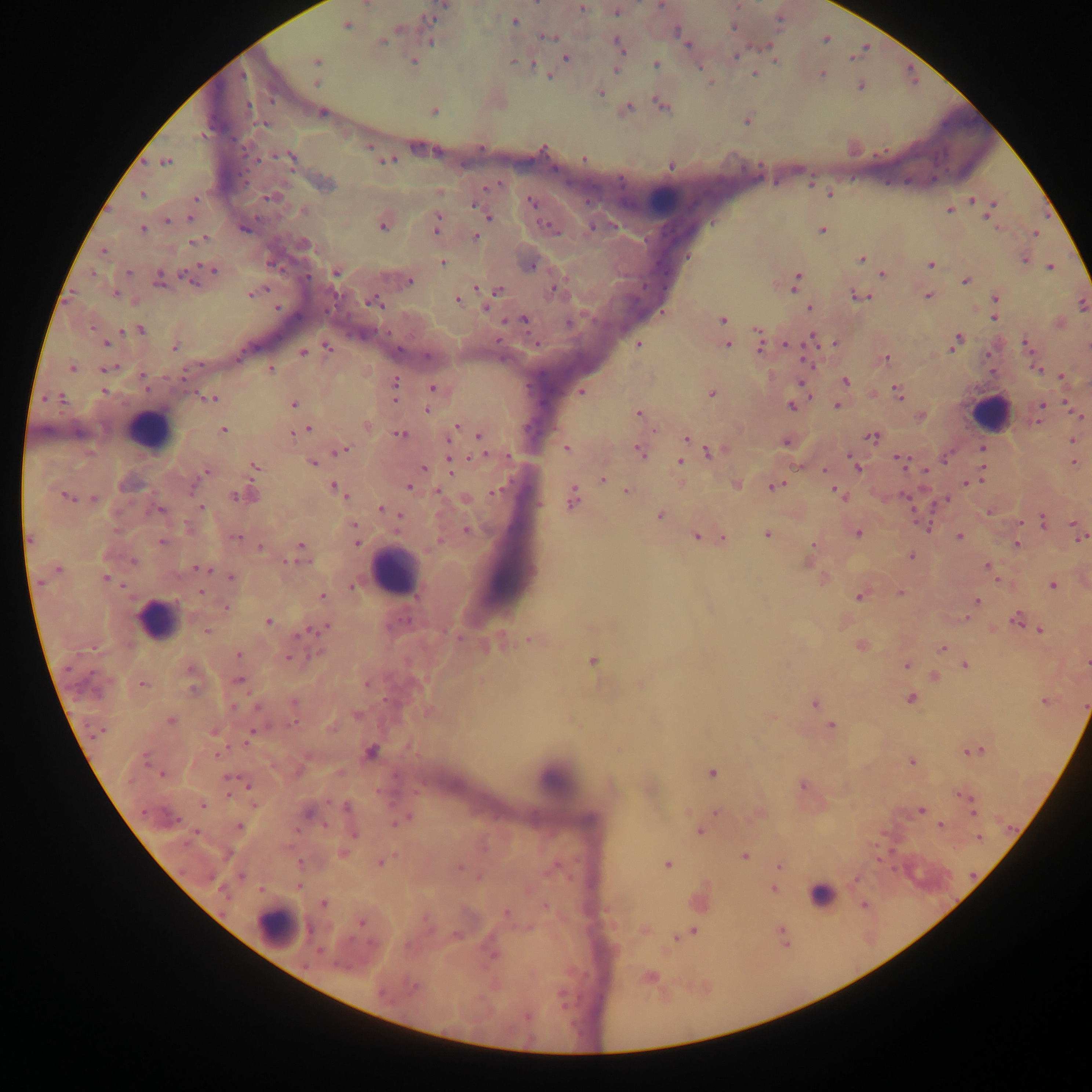 Approximate centers as [x, y] in pixels. Leukocyte locations: [663, 200], [989, 413], [149, 430], [393, 571], [158, 619], [822, 894], [277, 928]. Plasmodium parasite locations: [366, 4], [660, 5], [442, 6], [581, 8], [617, 11], [432, 19], [515, 21], [346, 26], [733, 27], [678, 33], [548, 37], [825, 39], [382, 42], [431, 42], [686, 43], [619, 44], [735, 55], [566, 59], [776, 60], [316, 61], [413, 62], [514, 62], [655, 65], [617, 69], [754, 74], [822, 75], [549, 78], [317, 83], [861, 86], [601, 92], [662, 105], [628, 109], [434, 111], [322, 112], [747, 121], [264, 124], [370, 146], [290, 158], [583, 159], [387, 160], [166, 162], [671, 166], [491, 187], [142, 194], [829, 194], [272, 197], [195, 198], [973, 200], [531, 201], [475, 205], [992, 205], [303, 211], [949, 211], [488, 215], [989, 216], [190, 219], [167, 221], [383, 226], [436, 226], [594, 226], [244, 228], [550, 228], [142, 229], [822, 230], [1035, 234], [476, 237], [198, 240], [103, 251], [861, 258], [1025, 260], [443, 263], [931, 265], [531, 266], [1050, 267], [214, 270], [128, 273], [336, 273], [882, 273], [93, 274], [184, 276], [158, 280], [966, 280], [409, 281], [796, 282], [554, 289], [498, 290], [116, 293], [253, 293], [859, 295], [928, 295], [996, 298], [458, 300], [374, 303], [1082, 305], [277, 308], [485, 308], [809, 309], [663, 312], [995, 317], [722, 320], [524, 321], [568, 323], [140, 330], [757, 330], [811, 339], [105, 343], [834, 343], [956, 343], [760, 344], [1026, 344], [638, 345], [728, 345], [786, 345], [175, 347], [327, 348], [304, 353], [426, 356], [238, 358], [887, 358], [71, 368], [106, 369], [1037, 369], [270, 370], [186, 373], [1061, 376], [144, 380], [846, 381], [395, 382], [146, 388], [433, 388], [395, 389], [103, 391], [581, 392], [899, 393], [712, 394], [53, 397], [46, 398], [61, 398], [211, 399], [395, 399], [294, 404], [837, 405], [1043, 405], [791, 406], [427, 410], [638, 414], [1078, 416], [920, 417], [367, 425], [456, 428], [309, 429], [223, 430], [295, 433], [401, 435], [479, 436], [686, 437], [872, 437], [1072, 440], [785, 443], [343, 449], [566, 449], [982, 449], [640, 451], [708, 452], [507, 456], [946, 458], [900, 460], [680, 462], [313, 463], [1074, 464], [451, 465], [255, 466], [855, 466], [424, 468], [824, 470], [206, 472], [926, 472], [980, 478], [602, 479], [967, 483], [736, 485], [775, 486], [409, 487], [334, 488], [497, 491], [627, 491], [439, 492], [253, 495], [841, 495], [65, 496], [239, 497], [573, 497], [93, 498], [945, 501], [201, 507], [382, 509], [160, 511], [989, 512], [398, 515], [660, 516], [1043, 521], [1073, 524], [354, 526], [925, 527], [467, 530], [857, 533], [768, 534], [697, 536], [236, 537], [960, 537], [1081, 538], [30, 539], [723, 539], [162, 541], [357, 543], [812, 545], [1016, 545], [302, 546], [261, 548], [911, 556], [133, 561], [987, 566], [200, 568], [58, 569], [231, 578], [105, 579], [1053, 586], [351, 587], [201, 593], [900, 593], [322, 596], [859, 597], [977, 601], [225, 608], [965, 619], [1016, 619], [268, 622], [317, 629], [1041, 630], [207, 632], [301, 633], [530, 639], [862, 646], [942, 649], [239, 655], [289, 657], [592, 661], [1087, 663], [906, 665], [965, 665], [191, 671], [934, 676], [238, 680], [143, 684], [367, 684], [193, 689], [911, 698], [1045, 701], [294, 703], [814, 703], [257, 707], [234, 708], [356, 715], [171, 721], [294, 722], [831, 725], [214, 731], [99, 732], [250, 735], [246, 741], [973, 750], [371, 752], [218, 754], [145, 760], [912, 762], [712, 772], [161, 774], [230, 779], [247, 784], [803, 786], [967, 797], [255, 804], [203, 805], [346, 806], [972, 809], [921, 810], [716, 812], [308, 813], [404, 819], [239, 826], [941, 826], [699, 832], [195, 833], [354, 835], [979, 839], [744, 855], [380, 862], [667, 865], [459, 867], [778, 867], [241, 875], [855, 879], [299, 886], [773, 889], [324, 904], [864, 905], [546, 907], [506, 913], [361, 922], [695, 932], [676, 938], [494, 955], [650, 978], [413, 988], [527, 1016]. Thick blood smear. Single field of view. Image is 1092×1092 pixels. Sample from Ghana. Mobile-phone photograph taken through the microscope.